Describe the morphology of the erythrocytes.
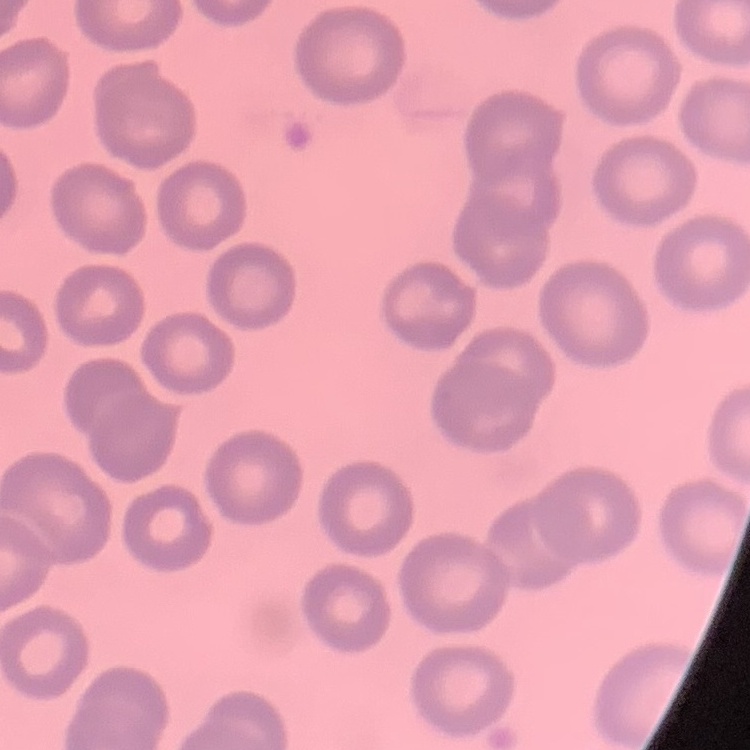

They show no rouleaux formation.

Thin blood smear. Square crop of a larger photomicrograph. Stained with either Field's or Giemsa.